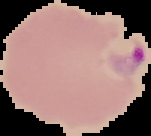

Summary:
  - Result: malaria parasites detected
  - Image type: cell region segmented out of the field of view; surrounding area masked to black
  - Image size: 151×136 pixels
  - Preparation: thin blood film